State the blood parasite species.
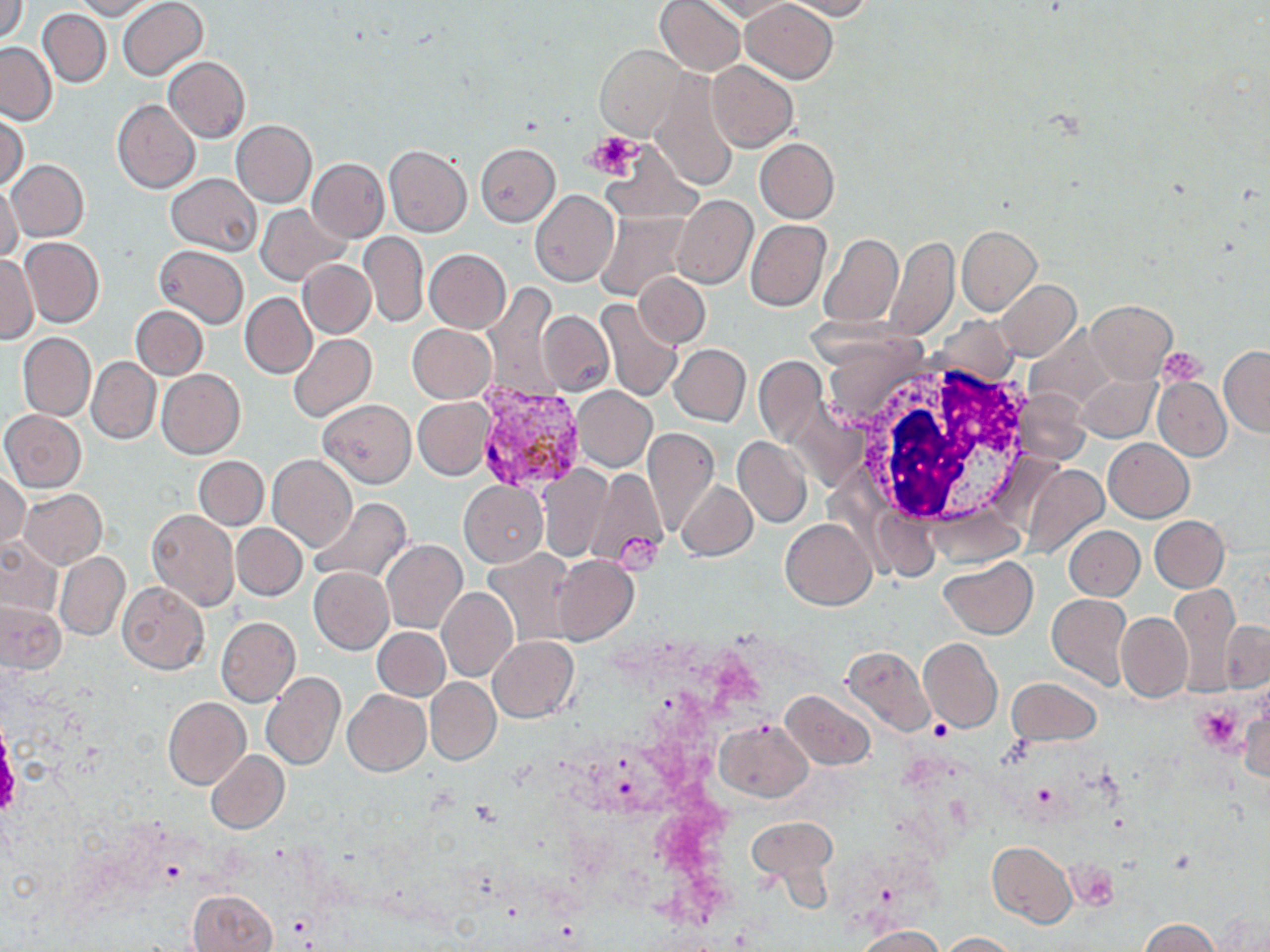
Plasmodium vivax.

Summary:
  - Coordinate format: approximate bounding boxes as [x1, y1, x2, y2] in pixels
  - White blood cell locations: [842, 356, 1043, 539]
  - Uninfected red blood cell locations: [1, 0, 29, 44], [74, 0, 159, 20], [118, 0, 208, 81], [656, 0, 746, 76], [786, 0, 872, 20], [703, 1, 798, 21], [741, 1, 837, 83], [38, 8, 112, 87], [0, 42, 56, 126], [595, 45, 687, 138], [165, 56, 249, 143], [707, 60, 797, 151], [650, 73, 740, 190], [112, 98, 199, 193], [1, 112, 28, 191], [232, 120, 317, 206], [755, 138, 839, 223], [598, 139, 704, 224], [475, 142, 559, 225], [384, 145, 471, 237], [306, 159, 388, 243], [6, 160, 89, 241], [166, 173, 261, 256], [0, 182, 23, 263], [530, 189, 619, 286], [672, 194, 756, 289], [258, 204, 349, 285], [595, 211, 690, 302], [746, 219, 832, 311], [957, 226, 1041, 314], [359, 232, 429, 327], [818, 233, 903, 329], [20, 237, 103, 327], [886, 237, 958, 337], [155, 246, 248, 328], [423, 248, 511, 333], [0, 255, 38, 343], [298, 260, 375, 338], [633, 272, 710, 347], [993, 280, 1081, 361], [483, 285, 560, 400], [241, 294, 316, 378], [595, 299, 684, 405], [1087, 300, 1176, 385], [132, 306, 208, 380], [540, 311, 613, 394], [407, 324, 495, 402], [18, 333, 96, 421], [288, 334, 376, 424], [669, 344, 750, 425], [1219, 345, 1270, 436], [86, 356, 161, 445], [754, 356, 829, 448], [156, 369, 245, 459], [1153, 376, 1230, 461], [572, 386, 656, 471], [413, 397, 494, 480], [318, 400, 415, 487], [1, 410, 85, 492], [644, 428, 718, 538], [734, 436, 812, 528], [1103, 438, 1193, 522], [194, 456, 268, 531], [267, 456, 357, 552], [1022, 465, 1107, 560], [538, 466, 615, 560], [583, 468, 668, 571], [0, 472, 30, 556], [676, 480, 757, 561], [459, 481, 548, 567], [19, 489, 106, 569], [307, 496, 413, 584], [146, 508, 239, 611], [1150, 516, 1229, 592], [781, 518, 875, 610], [232, 524, 306, 600], [1064, 525, 1145, 600], [0, 538, 63, 619], [381, 540, 466, 634], [484, 549, 577, 644], [53, 551, 130, 641], [550, 554, 638, 645], [938, 558, 1037, 638], [309, 566, 394, 654], [117, 581, 209, 675], [1170, 585, 1242, 687], [437, 588, 518, 682], [1046, 593, 1131, 689], [1, 601, 64, 673], [1116, 612, 1192, 702], [216, 616, 301, 707], [1220, 619, 1270, 693], [372, 628, 449, 700], [488, 636, 579, 722], [918, 639, 1001, 733], [840, 644, 934, 736], [262, 672, 346, 771], [425, 677, 501, 763], [1006, 678, 1100, 745], [342, 690, 430, 776], [781, 690, 875, 770], [1239, 691, 1269, 784], [163, 697, 250, 789], [715, 718, 813, 802], [206, 750, 289, 834], [746, 817, 835, 890], [987, 842, 1079, 928], [187, 889, 277, 952], [1139, 918, 1218, 952], [857, 926, 943, 952], [937, 932, 1020, 951]
  - Plasmodium vivax-infected red blood cell locations: [474, 379, 591, 493]
  - Platelet locations: [588, 132, 640, 178], [1158, 349, 1207, 387], [615, 534, 664, 573], [1197, 702, 1242, 753], [928, 720, 952, 742], [470, 800, 502, 827]
  - Modality: optical microscopy
  - Magnification: 1000x
  - Stain: May-Grünwald-Giemsa
  - Preparation: thin blood film
  - Image size: 1270×952 pixels
  - Field of view: single